Name the cell type shown.
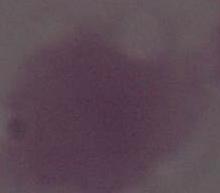
This is an erythrocyte.

modality = micrograph
magnification = 1000x